Find each parasitized RBC.
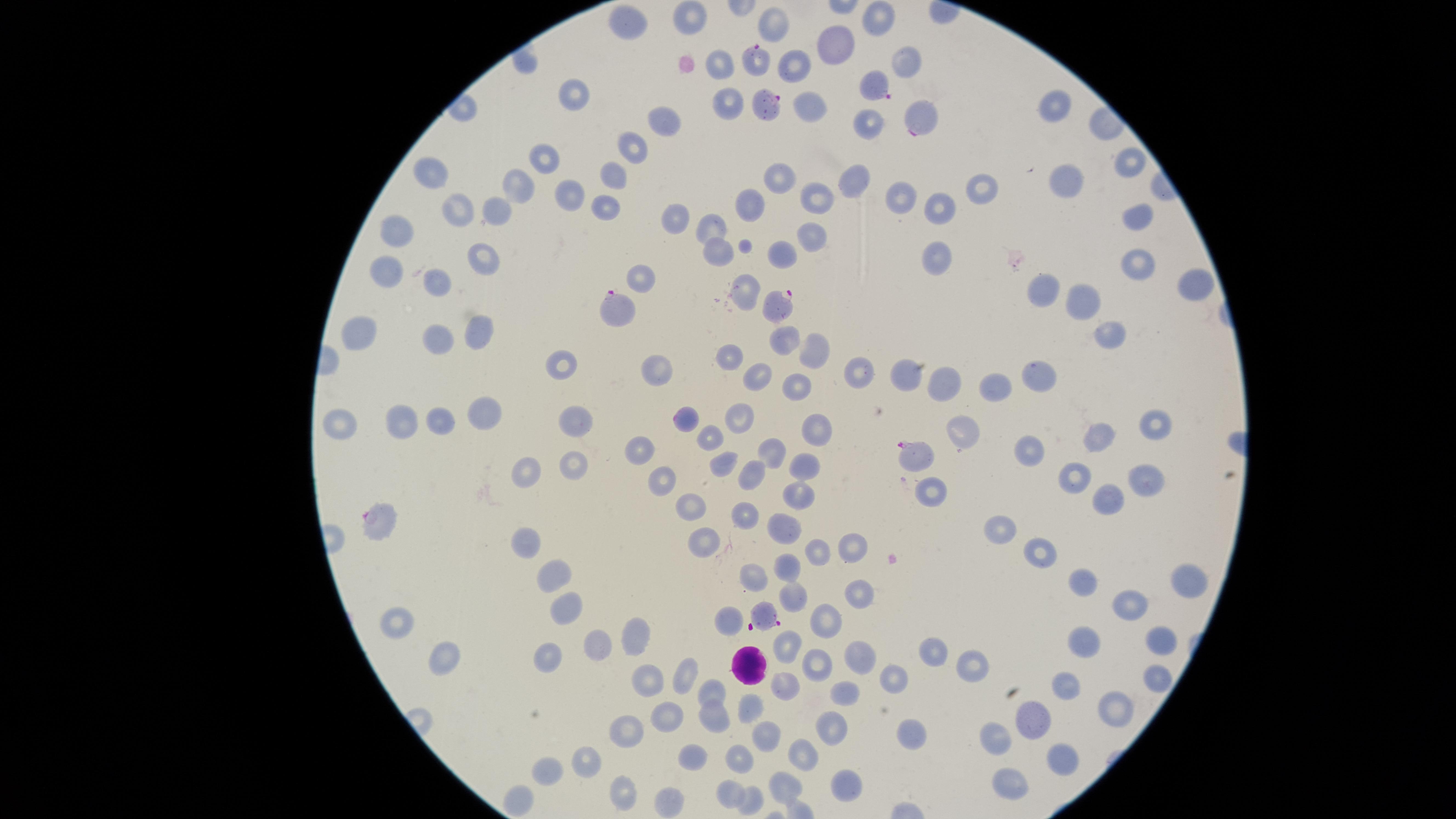

Approximate marker points, in pixels from the top-left corner.
Parasitized RBCs: (x=761, y=63), (x=881, y=90), (x=762, y=104), (x=925, y=121), (x=773, y=304), (x=618, y=306), (x=911, y=454), (x=379, y=519), (x=766, y=613).

Approximate marker points, in pixels from the top-left corner. Uninfected RBCs: (x=688, y=16), (x=883, y=18), (x=627, y=31), (x=836, y=43), (x=907, y=59), (x=794, y=63), (x=720, y=64), (x=577, y=95), (x=728, y=101), (x=810, y=101), (x=1054, y=104), (x=661, y=122), (x=873, y=122), (x=637, y=148), (x=544, y=157), (x=1128, y=161), (x=432, y=172), (x=615, y=174), (x=779, y=175), (x=850, y=175), (x=1065, y=180), (x=978, y=181), (x=523, y=185), (x=568, y=196), (x=821, y=198), (x=599, y=199), (x=900, y=199), (x=752, y=204), (x=503, y=205), (x=937, y=207), (x=458, y=209), (x=1136, y=212), (x=671, y=227), (x=402, y=229), (x=709, y=229), (x=810, y=233), (x=716, y=252), (x=780, y=254), (x=489, y=257), (x=936, y=257), (x=1136, y=260), (x=391, y=271), (x=643, y=276), (x=446, y=284), (x=1050, y=285), (x=1193, y=289), (x=748, y=291), (x=1084, y=302), (x=369, y=331), (x=1110, y=333), (x=441, y=338), (x=473, y=338), (x=779, y=338), (x=815, y=344), (x=733, y=350), (x=566, y=368), (x=906, y=369), (x=1034, y=369), (x=659, y=373), (x=857, y=373), (x=945, y=375), (x=757, y=376), (x=1001, y=378), (x=798, y=381), (x=493, y=414), (x=745, y=414), (x=685, y=418), (x=401, y=421), (x=337, y=423), (x=444, y=423), (x=1153, y=423), (x=576, y=425), (x=963, y=426), (x=816, y=430), (x=708, y=436), (x=1099, y=437), (x=636, y=446), (x=1025, y=449), (x=768, y=454), (x=725, y=460), (x=811, y=463), (x=569, y=464), (x=526, y=472), (x=747, y=474), (x=1078, y=476), (x=1144, y=481), (x=661, y=483), (x=933, y=490), (x=799, y=493), (x=1107, y=498), (x=690, y=507), (x=743, y=515), (x=785, y=521), (x=1004, y=524), (x=530, y=540), (x=706, y=541), (x=858, y=546), (x=1043, y=550), (x=814, y=551), (x=793, y=567), (x=556, y=574), (x=754, y=574), (x=1080, y=578), (x=1183, y=579), (x=853, y=582), (x=793, y=598), (x=1127, y=601), (x=571, y=607), (x=723, y=619), (x=825, y=619), (x=397, y=622), (x=1086, y=634), (x=636, y=636), (x=1159, y=638), (x=787, y=642), (x=601, y=643), (x=939, y=652), (x=863, y=655), (x=551, y=656), (x=445, y=657), (x=816, y=663), (x=976, y=667), (x=684, y=673), (x=895, y=678), (x=1155, y=681), (x=1068, y=682), (x=644, y=683), (x=787, y=685), (x=714, y=692), (x=842, y=694), (x=1116, y=702), (x=757, y=705), (x=667, y=715), (x=715, y=717), (x=1036, y=718), (x=625, y=725), (x=829, y=726), (x=763, y=732), (x=912, y=734), (x=996, y=734), (x=802, y=750), (x=1061, y=756), (x=694, y=759), (x=589, y=760), (x=744, y=761), (x=546, y=770), (x=853, y=777), (x=1007, y=779), (x=783, y=786), (x=733, y=787), (x=617, y=788), (x=756, y=796), (x=517, y=797), (x=670, y=799). WBCs: (x=744, y=662). Photographed with a smartphone camera through the microscope eyepiece. Thin blood film. One field of view of the specimen. Circular visible region. Species: Plasmodium falciparum. Giemsa stain. Image is 1456×819 pixels.